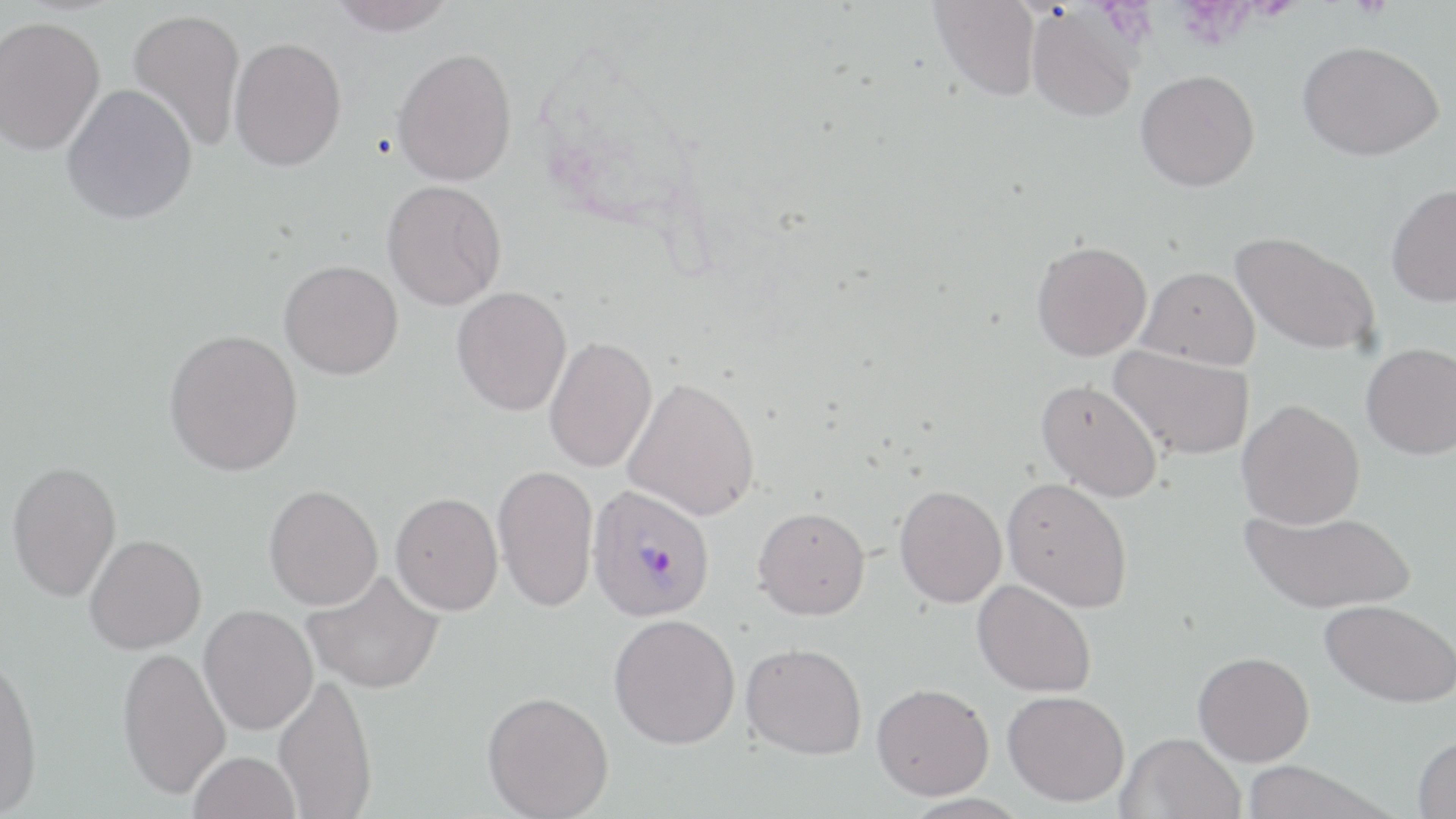

Approximate bounding boxes as named x1/y1/x2/y2 corners in pixels. Plasmodium vivax-infected red blood cell locations: (x1=586, y1=485, x2=716, y2=622). Uninfected red blood cell locations: (x1=328, y1=0, x2=459, y2=36), (x1=929, y1=1, x2=1041, y2=101), (x1=1026, y1=6, x2=1141, y2=122), (x1=128, y1=8, x2=246, y2=153), (x1=0, y1=16, x2=105, y2=155), (x1=229, y1=37, x2=346, y2=171), (x1=1297, y1=39, x2=1444, y2=161), (x1=391, y1=47, x2=517, y2=186), (x1=1135, y1=69, x2=1260, y2=191), (x1=62, y1=84, x2=198, y2=225), (x1=381, y1=180, x2=506, y2=310), (x1=1386, y1=184, x2=1456, y2=307), (x1=1230, y1=230, x2=1380, y2=356), (x1=1031, y1=240, x2=1151, y2=361), (x1=279, y1=259, x2=403, y2=380), (x1=1137, y1=266, x2=1260, y2=369), (x1=451, y1=286, x2=571, y2=416), (x1=164, y1=328, x2=303, y2=476), (x1=544, y1=336, x2=657, y2=473), (x1=1361, y1=342, x2=1456, y2=460), (x1=1108, y1=345, x2=1255, y2=459), (x1=623, y1=377, x2=760, y2=521), (x1=1036, y1=378, x2=1162, y2=502), (x1=1237, y1=399, x2=1365, y2=529), (x1=7, y1=460, x2=122, y2=602), (x1=493, y1=463, x2=599, y2=613), (x1=1002, y1=476, x2=1133, y2=612), (x1=264, y1=484, x2=383, y2=610), (x1=894, y1=484, x2=1007, y2=608), (x1=390, y1=492, x2=503, y2=615), (x1=752, y1=506, x2=870, y2=620), (x1=1241, y1=507, x2=1417, y2=614), (x1=84, y1=534, x2=206, y2=654), (x1=304, y1=569, x2=445, y2=695), (x1=972, y1=579, x2=1096, y2=697), (x1=1319, y1=598, x2=1456, y2=708), (x1=199, y1=604, x2=318, y2=736), (x1=608, y1=613, x2=740, y2=749), (x1=741, y1=642, x2=867, y2=759), (x1=117, y1=645, x2=231, y2=799), (x1=0, y1=650, x2=43, y2=816), (x1=1193, y1=651, x2=1314, y2=766), (x1=273, y1=673, x2=377, y2=819), (x1=872, y1=682, x2=994, y2=799), (x1=1003, y1=690, x2=1129, y2=806), (x1=482, y1=691, x2=614, y2=818), (x1=1117, y1=732, x2=1245, y2=819), (x1=1413, y1=734, x2=1456, y2=818), (x1=189, y1=751, x2=302, y2=819), (x1=1240, y1=761, x2=1393, y2=819). Slide-level diagnosis: Plasmodium vivax. Captured at 1000x magnification. May-Grünwald-Giemsa stain. Image is 1456×819 pixels. Thin blood smear. One field of a larger specimen. Optical microscopy.